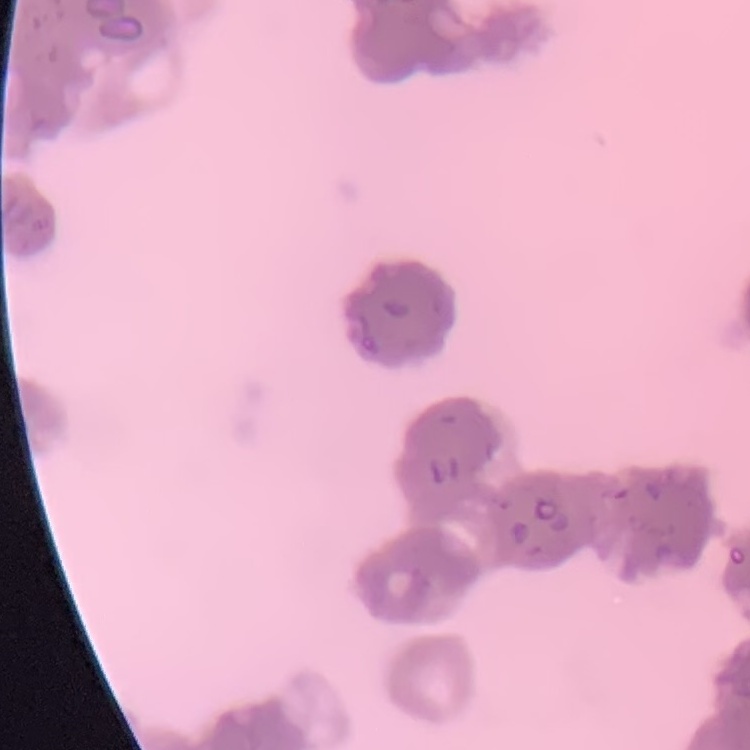
The red blood cells show rouleaux formation. Square crop of a larger photomicrograph. Thin blood smear. Stained with either Field's or Giemsa.